Classify this cell by malaria status.
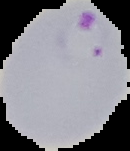

Parasitized.

{
  "image_size": "130×151 pixels",
  "image_type": "cell region segmented out of the field of view; surrounding area masked to black",
  "preparation": "thin blood smear"
}